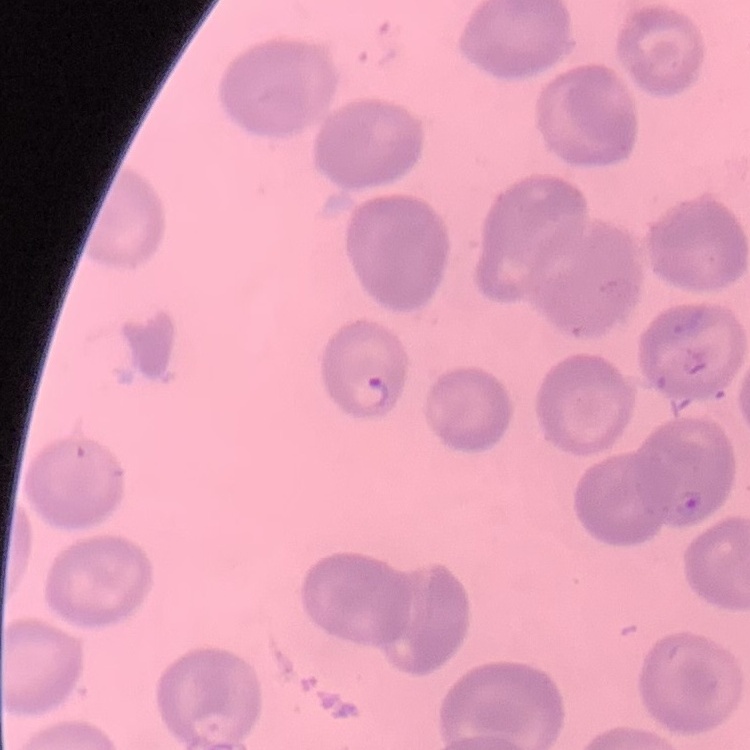
The red blood cells exhibit no rouleaux formation. Thin blood smear. Stained with either Field's or Giemsa. Square crop of a larger photomicrograph.